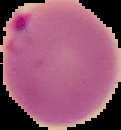 Result: Plasmodium parasites detected. The area outside the segmented cell region is set to black. Image is 121×130 pixels. From a thin blood film.